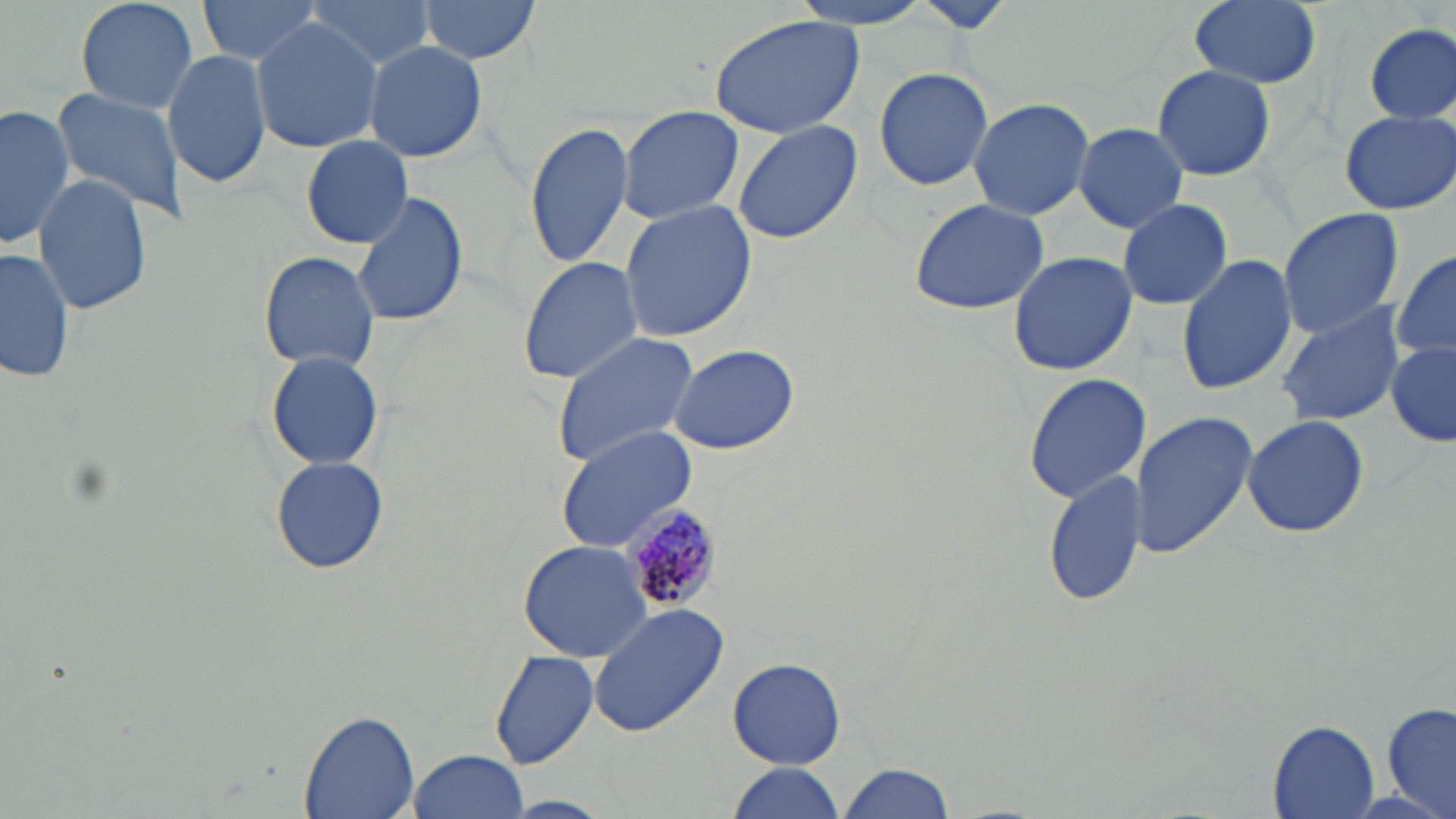 Approximate bounding boxes as named x1/y1/x2/y2 corners in pixels. Plasmodium malariae-infected red blood cell locations: (x1=621, y1=508, x2=721, y2=616). Uninfected red blood cell locations: (x1=75, y1=0, x2=202, y2=115), (x1=199, y1=0, x2=329, y2=66), (x1=300, y1=0, x2=439, y2=65), (x1=418, y1=0, x2=545, y2=65), (x1=787, y1=0, x2=939, y2=30), (x1=1187, y1=1, x2=1320, y2=89), (x1=913, y1=2, x2=1019, y2=35), (x1=706, y1=15, x2=869, y2=138), (x1=251, y1=18, x2=381, y2=154), (x1=1363, y1=22, x2=1456, y2=125), (x1=362, y1=41, x2=487, y2=163), (x1=163, y1=46, x2=271, y2=189), (x1=1151, y1=64, x2=1277, y2=181), (x1=872, y1=66, x2=994, y2=191), (x1=47, y1=87, x2=189, y2=225), (x1=966, y1=97, x2=1096, y2=219), (x1=0, y1=102, x2=75, y2=250), (x1=617, y1=106, x2=746, y2=228), (x1=1339, y1=109, x2=1455, y2=215), (x1=731, y1=118, x2=864, y2=245), (x1=525, y1=120, x2=636, y2=269), (x1=1074, y1=122, x2=1188, y2=234), (x1=301, y1=136, x2=413, y2=248), (x1=33, y1=172, x2=153, y2=318), (x1=350, y1=191, x2=470, y2=327), (x1=906, y1=197, x2=1052, y2=315), (x1=1116, y1=197, x2=1233, y2=311), (x1=619, y1=200, x2=757, y2=343), (x1=1275, y1=208, x2=1407, y2=339), (x1=1, y1=244, x2=75, y2=388), (x1=1389, y1=248, x2=1456, y2=366), (x1=260, y1=250, x2=379, y2=372), (x1=1008, y1=250, x2=1136, y2=376), (x1=1175, y1=253, x2=1299, y2=397), (x1=517, y1=254, x2=645, y2=386), (x1=1276, y1=300, x2=1405, y2=427), (x1=550, y1=333, x2=700, y2=469), (x1=1387, y1=342, x2=1456, y2=449), (x1=665, y1=343, x2=800, y2=456), (x1=266, y1=350, x2=384, y2=472), (x1=1021, y1=373, x2=1149, y2=504), (x1=1132, y1=410, x2=1258, y2=560), (x1=1241, y1=415, x2=1369, y2=538), (x1=555, y1=425, x2=701, y2=554), (x1=269, y1=456, x2=389, y2=574), (x1=1044, y1=468, x2=1146, y2=610), (x1=518, y1=539, x2=656, y2=663), (x1=589, y1=602, x2=732, y2=739), (x1=490, y1=650, x2=598, y2=770), (x1=728, y1=657, x2=846, y2=769), (x1=1382, y1=702, x2=1456, y2=818), (x1=299, y1=712, x2=419, y2=819), (x1=1266, y1=720, x2=1381, y2=819), (x1=403, y1=749, x2=528, y2=819), (x1=724, y1=763, x2=846, y2=819), (x1=834, y1=763, x2=955, y2=819). Slide-level diagnosis: Plasmodium malariae. May-Grünwald-Giemsa stain. Thin blood smear. Optical microscopy. One field of a larger specimen. 1000x magnification. Image is 1456×819 pixels.